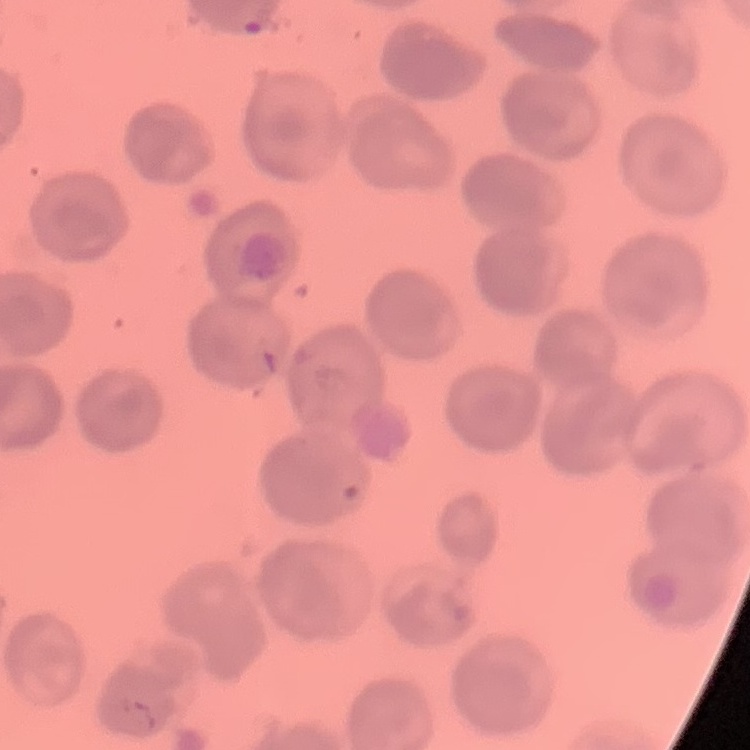
red blood cell morphology = no rouleaux formation
stain = Field's or Giemsa
image type = square crop of a larger photomicrograph
preparation = thin peripheral smear